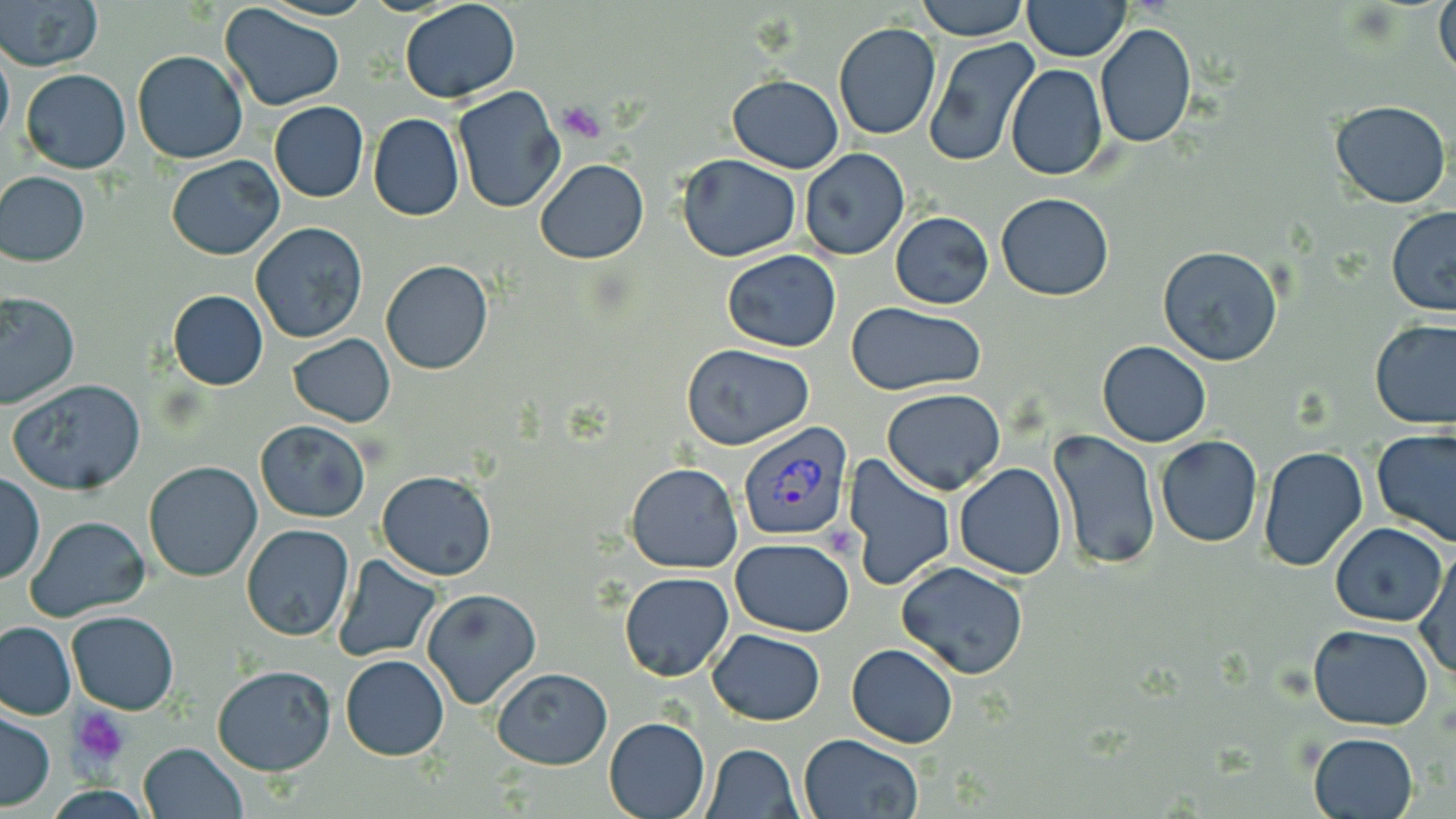 Approximate bounding boxes as [x1, y1, x2, y2] in pixels. Platelet locations: [558, 99, 605, 138], [72, 710, 131, 766]. Uninfected red blood cell locations: [1, 0, 102, 73], [916, 0, 1029, 41], [1025, 0, 1129, 60], [1433, 0, 1455, 85], [399, 1, 523, 104], [219, 3, 346, 112], [831, 23, 942, 142], [1095, 23, 1196, 149], [922, 37, 1041, 169], [0, 42, 13, 152], [132, 49, 247, 165], [1005, 64, 1108, 180], [21, 68, 131, 175], [727, 75, 845, 172], [450, 85, 566, 214], [1329, 100, 1451, 209], [268, 101, 368, 202], [367, 114, 464, 222], [798, 149, 910, 262], [675, 154, 801, 261], [166, 155, 285, 259], [535, 159, 648, 264], [0, 173, 90, 266], [996, 192, 1113, 302], [1386, 207, 1456, 314], [890, 211, 993, 309], [251, 221, 368, 345], [1158, 244, 1286, 367], [722, 249, 841, 351], [379, 259, 494, 375], [167, 289, 269, 391], [0, 292, 78, 409], [848, 304, 990, 395], [1370, 321, 1456, 431], [287, 333, 396, 428], [1097, 341, 1211, 447], [682, 343, 815, 449], [8, 379, 149, 496], [881, 388, 1005, 495], [254, 420, 373, 523], [1048, 429, 1162, 570], [1372, 430, 1456, 548], [1154, 434, 1263, 548], [1259, 445, 1369, 572], [845, 454, 956, 592], [144, 461, 263, 582], [625, 461, 744, 573], [954, 463, 1068, 581], [376, 470, 497, 579], [1, 471, 45, 586], [25, 515, 149, 623], [241, 523, 354, 641], [1330, 523, 1448, 628], [730, 538, 855, 635], [1414, 550, 1456, 681], [333, 555, 442, 661], [896, 562, 1029, 680], [619, 572, 735, 682], [422, 589, 542, 710], [67, 612, 178, 713], [0, 620, 76, 720], [1308, 625, 1436, 730], [706, 629, 826, 725], [845, 643, 959, 749], [340, 655, 450, 760], [212, 665, 335, 777], [492, 667, 613, 769], [0, 709, 54, 811], [604, 717, 710, 819], [1308, 732, 1418, 818], [798, 733, 924, 819], [137, 742, 248, 819], [701, 742, 802, 818]. Plasmodium vivax-infected red blood cell locations: [737, 421, 852, 539]. Slide-level diagnosis: Plasmodium vivax. Image is 1456×819 pixels. Single field of view. Thin blood film. 1000x magnification. May-Grünwald-Giemsa-stained preparation. Light microscopy.